State which parasite is depicted.
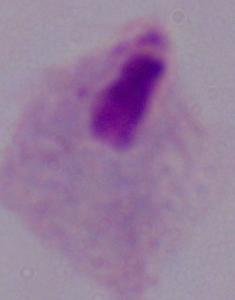

A trichomonad.

Summary:
  - Modality: micrograph
  - Magnification: 1000x